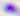 Photomicrograph. Toxoplasma gondii is seen. 400x magnification.